Assess this cell for malaria.
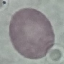

It is uninfected.

Summary:
  - Image type: automatically extracted cell patch, resized to 64 × 64 pixels
  - Stain: Giemsa
  - Preparation: thin smear
  - Capture: smartphone camera at the microscope eyepiece